Report the malaria status of this cell.
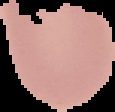
It is uninfected.

{
  "image_type": "segmented cell region with the area outside set to black",
  "preparation": "thin blood smear",
  "image_size": "115×112 pixels"
}